State the preparation type.
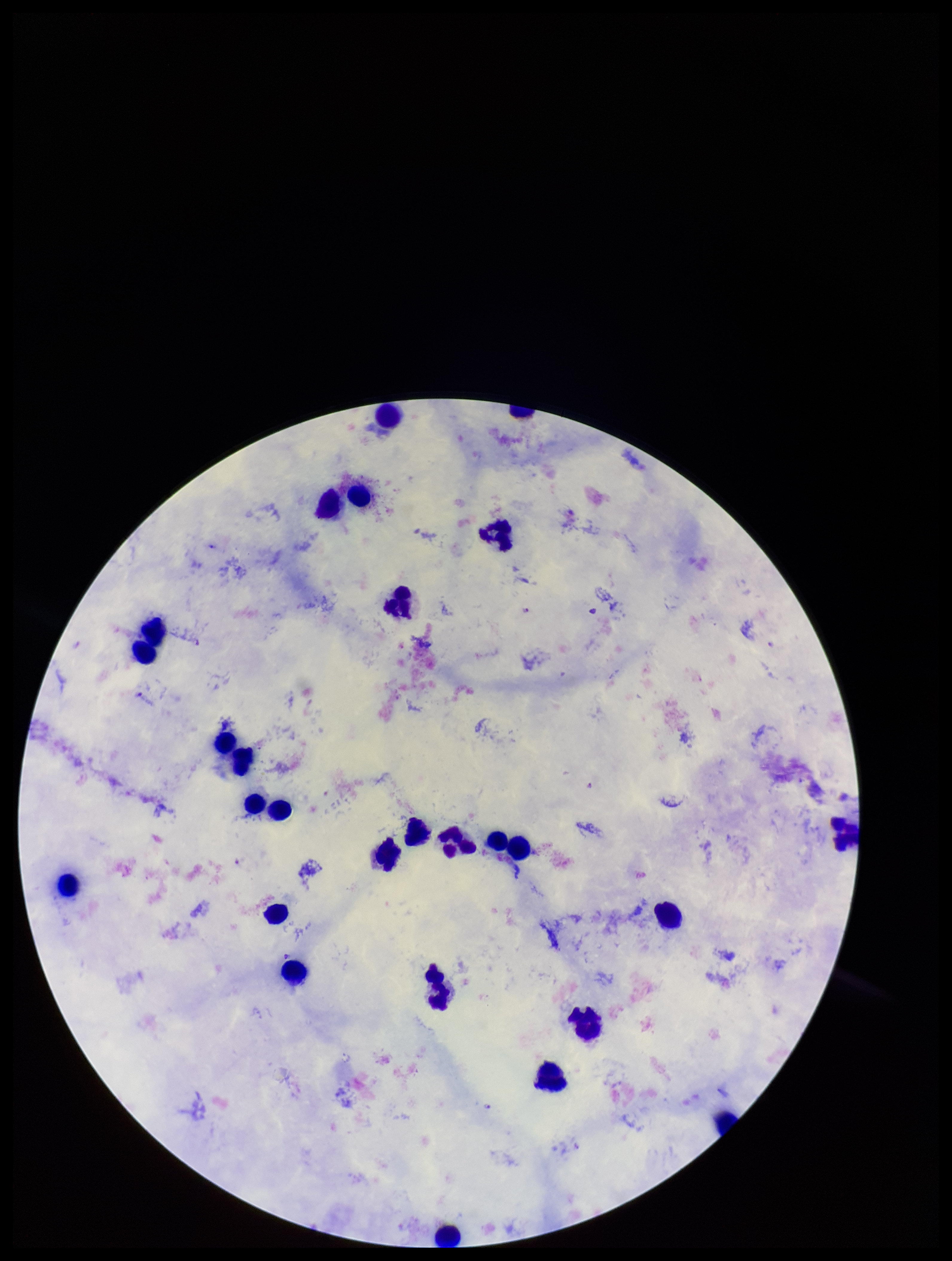

A thick smear.

Summary:
  - Plasmodium parasites: detected
  - Stain: Giemsa
  - Species reported for this patient: Plasmodium falciparum
  - Capture: smartphone photograph through the microscope eyepiece
  - Leukocyte count: 27
  - Image size: 952×1261 pixels
  - Patient malaria status: infected
  - Field of view: single
  - Parasite count: 4